Locate every leukocyte (white blood cell).
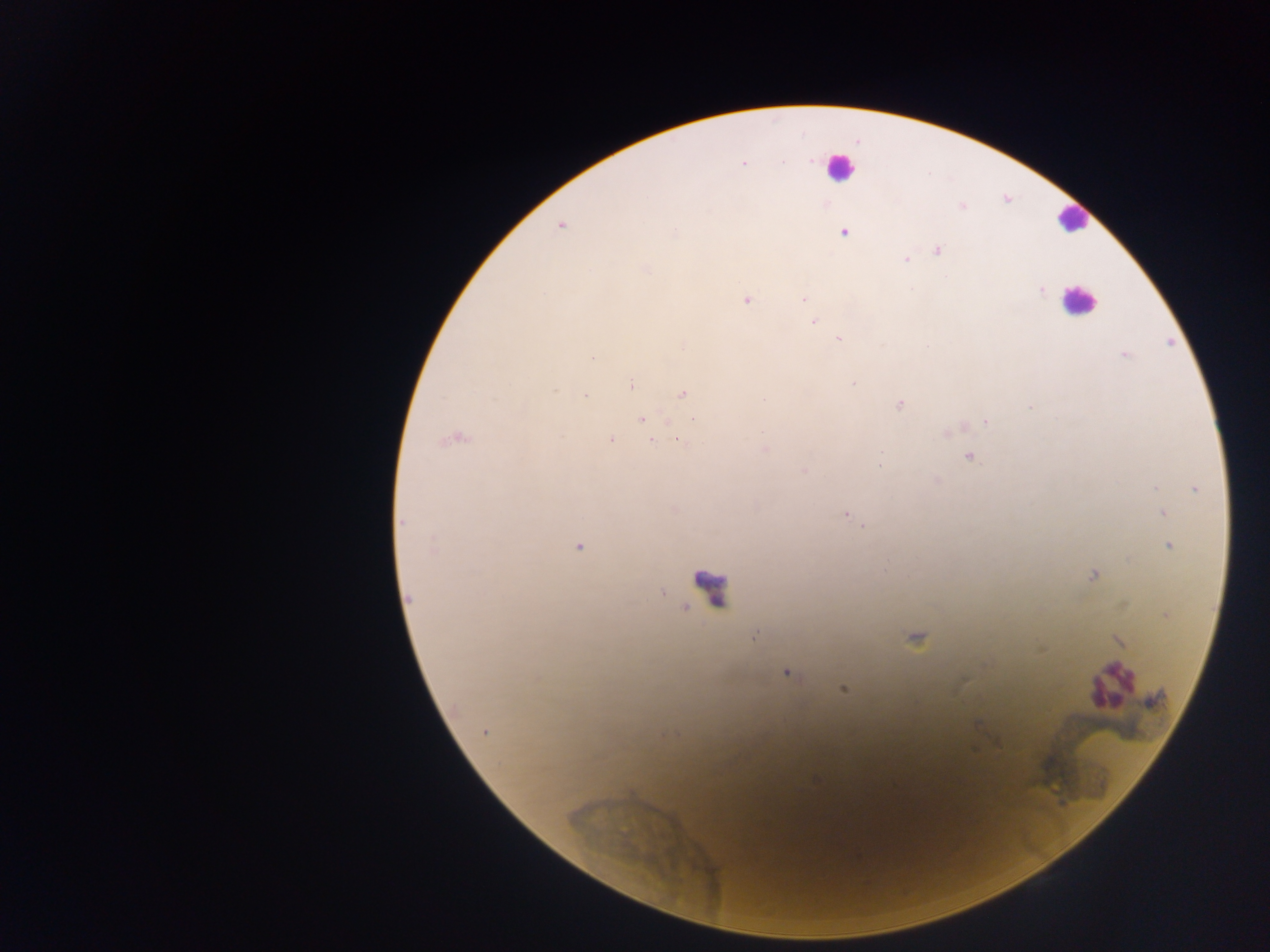
Approximate centers as {x, y} in pixels.
Leukocytes: {840, 168}, {1072, 219}, {1078, 301}, {709, 588}, {1108, 684}.

country = Ghana
field of view = single
capture = mobile-phone photograph through a microscope
malaria parasite locations = approximate centers as {x, y} in pixels: {742, 162}, {560, 225}, {843, 232}, {937, 249}, {906, 258}, {1041, 290}, {804, 298}, {747, 299}, {813, 321}, {839, 338}, {1124, 354}, {630, 384}, {852, 384}, {682, 394}, {585, 395}, {765, 399}, {899, 404}, {694, 417}, {642, 419}, {987, 421}, {454, 437}, {610, 439}, {652, 440}, {679, 440}, {764, 449}, {969, 455}, {804, 471}, {1155, 487}, {1195, 488}, {1163, 512}, {845, 514}, {863, 527}, {1169, 545}, {578, 546}, {1092, 574}, {661, 592}, {408, 599}, {686, 608}, {1166, 614}, {916, 639}, {1118, 640}, {787, 671}, {843, 688}, {975, 723}, {485, 731}
preparation = thick blood film
image size = 1270×952 pixels